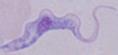

Photomicrograph. 1000x magnification. A trypanosome is seen.